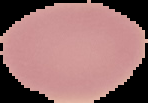
preparation: thin blood film
image_type: cell region segmented out of the field of view; surrounding area masked to black
image_size: 148×103 pixels
malaria_status: uninfected